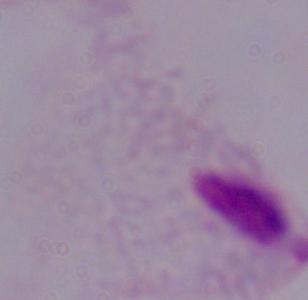
Micrograph. A trichomonad is seen. Captured at 1000x magnification.